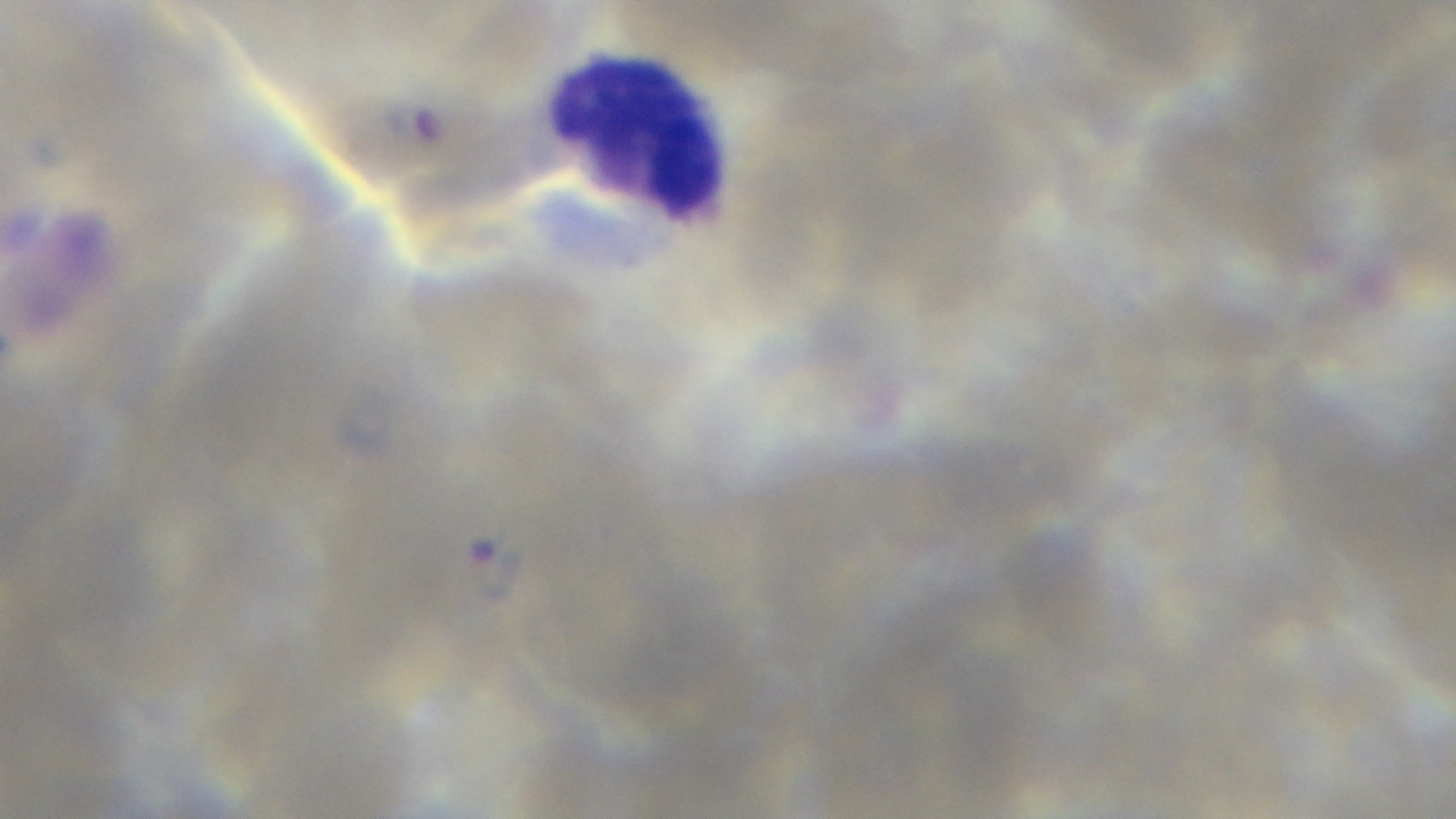
Single field of view. Malaria status: positive. Mounted 4K digital camera. Light microscopy. Giemsa stain. Preparation: thin. 100x oil-immersion objective.